Classify this cell by malaria status.
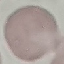

It is uninfected.

Thin blood smear. Giemsa stain. Cell patch, automatically extracted from a larger field of view and resized to 64 × 64 pixels. Acquired by smartphone through the microscope eyepiece.